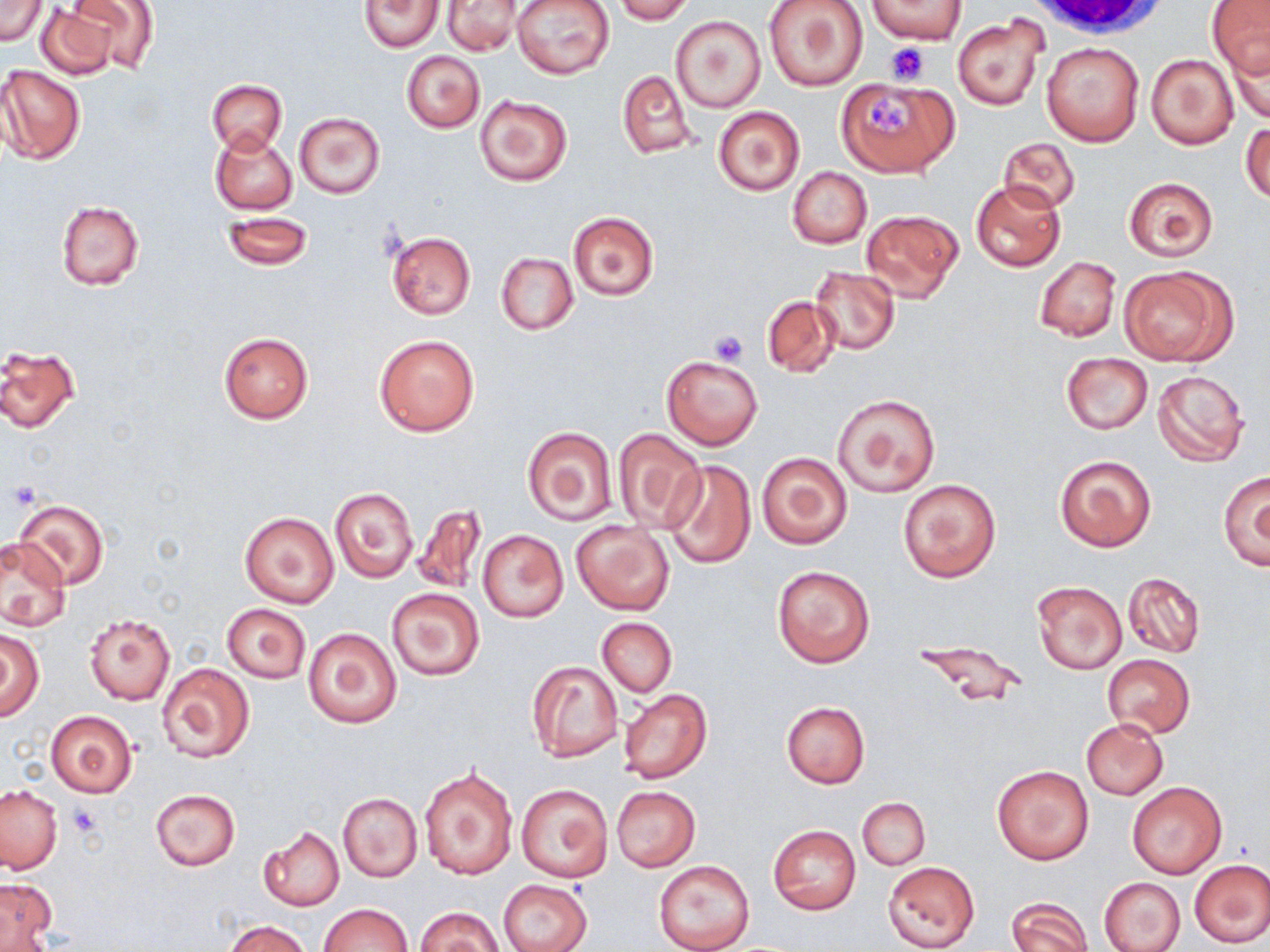
slide-level diagnosis = no evidence of blood parasites
magnification = 1000x
modality = optical microscopy
field of view = one of a larger specimen
uninfected red blood cell locations = approximate bounding boxes as [x1, y1, x2, y2] in pixels: [68, 0, 159, 73], [512, 0, 614, 80], [613, 0, 695, 24], [764, 0, 870, 92], [1209, 0, 1270, 79], [1, 1, 46, 45], [361, 1, 443, 52], [444, 1, 521, 55], [870, 1, 963, 45], [36, 3, 125, 80], [672, 16, 765, 112], [952, 16, 1047, 112], [1224, 31, 1269, 123], [1041, 42, 1143, 146], [402, 50, 484, 133], [1147, 52, 1240, 150], [1, 64, 86, 164], [615, 70, 695, 157], [836, 77, 956, 176], [207, 80, 286, 153], [476, 94, 572, 186], [712, 105, 805, 197], [294, 113, 385, 198], [1241, 120, 1269, 205], [211, 130, 297, 214], [996, 137, 1081, 214], [787, 166, 871, 249], [1122, 176, 1219, 261], [971, 179, 1065, 272], [55, 200, 144, 290], [861, 208, 963, 302], [221, 211, 313, 270], [568, 211, 659, 300], [386, 232, 476, 320], [495, 251, 578, 334], [1035, 256, 1121, 341], [1119, 265, 1237, 365], [809, 267, 900, 356], [762, 296, 840, 378], [219, 333, 313, 423], [374, 333, 481, 437], [1, 344, 80, 433], [1061, 352, 1152, 434], [662, 354, 763, 450], [1152, 369, 1251, 466], [832, 393, 941, 498], [522, 427, 617, 526], [613, 429, 706, 532], [755, 451, 852, 550], [1054, 454, 1156, 552], [662, 460, 757, 570], [1217, 469, 1270, 570], [897, 478, 1001, 583], [330, 487, 418, 582], [12, 497, 108, 592], [411, 505, 487, 596], [240, 511, 338, 608], [571, 522, 675, 615], [478, 529, 567, 623], [1, 536, 70, 631], [772, 565, 875, 667], [1124, 572, 1205, 658], [1032, 581, 1128, 675], [386, 588, 485, 681], [222, 603, 310, 683], [85, 612, 175, 706], [598, 618, 677, 696], [303, 627, 402, 728], [0, 631, 44, 720], [915, 640, 1026, 712], [1102, 654, 1194, 737], [525, 660, 623, 762], [157, 662, 254, 763], [618, 688, 711, 784], [782, 701, 870, 787], [43, 710, 139, 798], [1082, 718, 1168, 799], [992, 764, 1095, 865], [418, 765, 519, 881], [1127, 781, 1227, 878], [516, 783, 613, 882], [0, 784, 63, 874], [611, 787, 700, 871], [150, 788, 239, 871], [339, 793, 422, 881], [858, 797, 930, 870], [768, 824, 860, 915], [259, 826, 344, 911], [1188, 858, 1270, 949], [654, 860, 754, 952], [882, 861, 980, 951], [1099, 876, 1186, 952], [1, 879, 57, 948], [500, 879, 591, 952], [1006, 897, 1092, 952], [317, 903, 413, 952], [415, 906, 504, 952], [225, 919, 309, 952]
preparation = thin blood smear
platelet locations = approximate bounding boxes as [x1, y1, x2, y2] in pixels: [885, 43, 930, 85], [868, 97, 914, 138], [708, 327, 749, 365], [6, 482, 41, 510], [68, 804, 101, 838]
stain = May-Grünwald-Giemsa
image size = 1270×952 pixels
white blood cell locations = approximate bounding boxes as [x1, y1, x2, y2] in pixels: [1027, 0, 1175, 43]